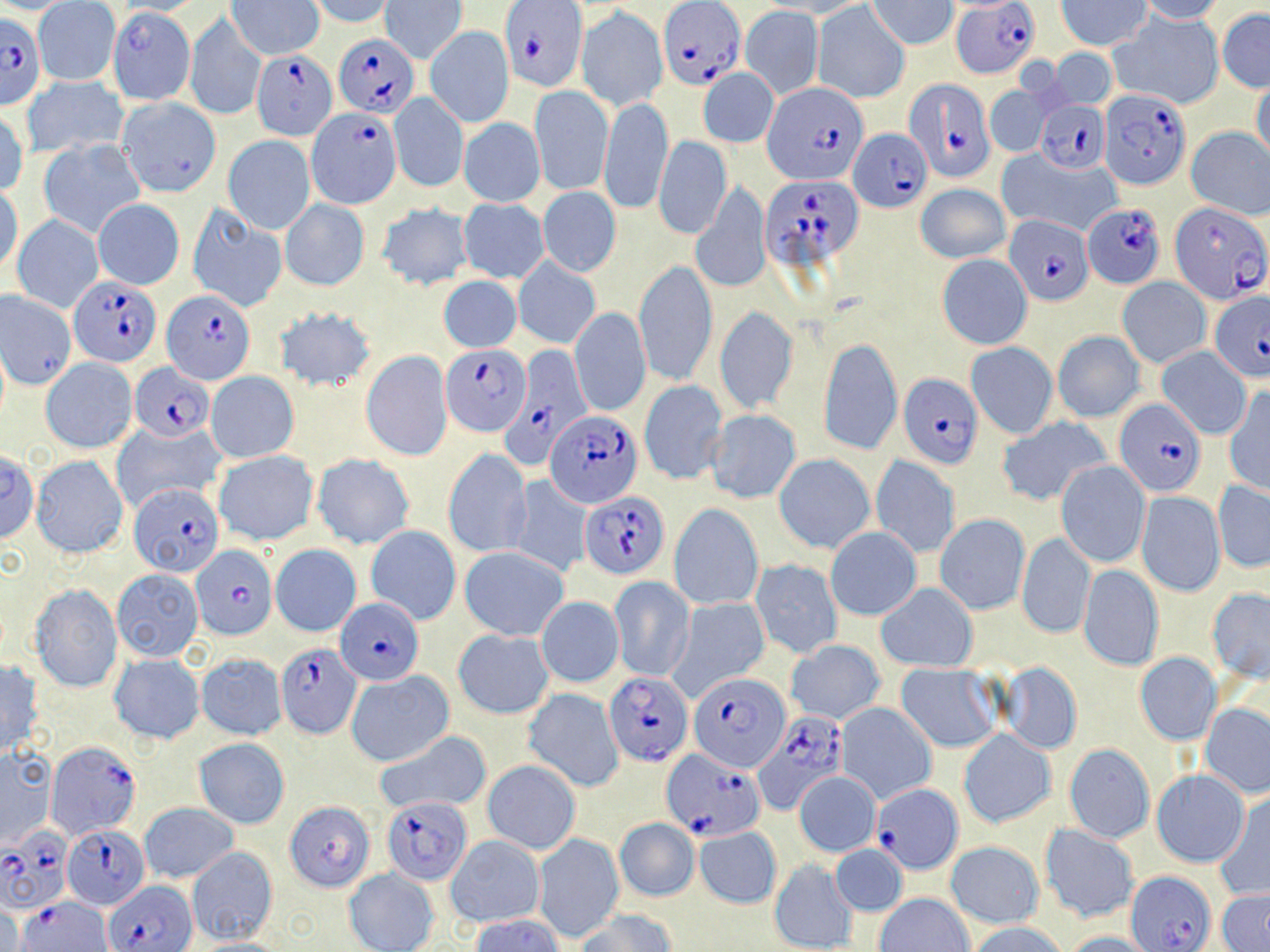
Summary:
  - Coordinate format: approximate bounding boxes as named x1/y1/x2/y2 corners in pixels
  - Plasmodium falciparum-infected red blood cell locations (subset): (x1=659, y1=0, x2=745, y2=88), (x1=500, y1=1, x2=586, y2=93), (x1=955, y1=1, x2=1037, y2=79), (x1=0, y1=11, x2=45, y2=111), (x1=333, y1=34, x2=419, y2=117), (x1=253, y1=49, x2=338, y2=141), (x1=764, y1=80, x2=866, y2=184), (x1=904, y1=80, x2=996, y2=185), (x1=1100, y1=89, x2=1193, y2=190), (x1=1036, y1=99, x2=1110, y2=176), (x1=309, y1=109, x2=400, y2=207), (x1=848, y1=130, x2=932, y2=212), (x1=761, y1=176, x2=862, y2=271), (x1=1083, y1=200, x2=1165, y2=287), (x1=1169, y1=200, x2=1269, y2=311), (x1=1005, y1=214, x2=1095, y2=305), (x1=70, y1=276, x2=162, y2=367), (x1=161, y1=290, x2=253, y2=384), (x1=1209, y1=291, x2=1270, y2=382), (x1=511, y1=343, x2=599, y2=458), (x1=442, y1=346, x2=528, y2=435), (x1=129, y1=362, x2=215, y2=441), (x1=898, y1=373, x2=984, y2=469), (x1=1115, y1=398, x2=1207, y2=497), (x1=545, y1=409, x2=642, y2=509), (x1=127, y1=482, x2=224, y2=577), (x1=580, y1=492, x2=670, y2=578), (x1=191, y1=544, x2=277, y2=639), (x1=335, y1=597, x2=424, y2=684), (x1=275, y1=642, x2=362, y2=738), (x1=688, y1=672, x2=791, y2=771), (x1=604, y1=673, x2=693, y2=765), (x1=754, y1=711, x2=849, y2=814), (x1=45, y1=740, x2=142, y2=839), (x1=660, y1=750, x2=764, y2=840), (x1=872, y1=784, x2=963, y2=873), (x1=382, y1=798, x2=473, y2=885), (x1=284, y1=801, x2=375, y2=891), (x1=61, y1=826, x2=149, y2=909), (x1=0, y1=832, x2=71, y2=912), (x1=1126, y1=871, x2=1216, y2=951), (x1=105, y1=880, x2=194, y2=951), (x1=20, y1=897, x2=114, y2=952)
  - Uninfected red blood cell locations (subset): (x1=762, y1=0, x2=872, y2=17), (x1=1056, y1=0, x2=1152, y2=51), (x1=1134, y1=0, x2=1226, y2=23), (x1=227, y1=1, x2=323, y2=59), (x1=307, y1=1, x2=398, y2=27), (x1=380, y1=1, x2=466, y2=63), (x1=867, y1=1, x2=956, y2=47), (x1=33, y1=2, x2=120, y2=85), (x1=740, y1=5, x2=822, y2=100), (x1=813, y1=5, x2=909, y2=103), (x1=107, y1=7, x2=194, y2=105), (x1=576, y1=7, x2=668, y2=112), (x1=1110, y1=7, x2=1225, y2=111), (x1=1216, y1=9, x2=1270, y2=93), (x1=185, y1=14, x2=265, y2=121), (x1=424, y1=26, x2=514, y2=128), (x1=1048, y1=49, x2=1117, y2=110), (x1=698, y1=68, x2=779, y2=149), (x1=21, y1=75, x2=127, y2=159), (x1=1250, y1=77, x2=1269, y2=167), (x1=985, y1=84, x2=1053, y2=157), (x1=530, y1=85, x2=614, y2=195), (x1=389, y1=93, x2=468, y2=194), (x1=599, y1=95, x2=672, y2=216), (x1=116, y1=97, x2=222, y2=197), (x1=1, y1=108, x2=28, y2=196), (x1=459, y1=119, x2=545, y2=207), (x1=1184, y1=126, x2=1270, y2=219), (x1=223, y1=134, x2=316, y2=234), (x1=653, y1=137, x2=731, y2=240), (x1=38, y1=138, x2=145, y2=239), (x1=998, y1=149, x2=1122, y2=237), (x1=692, y1=180, x2=772, y2=295), (x1=0, y1=183, x2=22, y2=277), (x1=916, y1=183, x2=1009, y2=264), (x1=537, y1=186, x2=621, y2=277), (x1=93, y1=198, x2=185, y2=290), (x1=457, y1=198, x2=549, y2=284), (x1=280, y1=199, x2=369, y2=291), (x1=186, y1=202, x2=287, y2=312), (x1=375, y1=202, x2=474, y2=292), (x1=12, y1=214, x2=104, y2=312), (x1=937, y1=255, x2=1032, y2=350), (x1=513, y1=258, x2=601, y2=348), (x1=633, y1=263, x2=718, y2=386), (x1=439, y1=275, x2=521, y2=352), (x1=1118, y1=277, x2=1210, y2=369), (x1=583, y1=285, x2=705, y2=402), (x1=273, y1=305, x2=378, y2=393), (x1=570, y1=306, x2=650, y2=417), (x1=713, y1=308, x2=799, y2=416), (x1=1052, y1=331, x2=1146, y2=423), (x1=820, y1=337, x2=903, y2=457), (x1=966, y1=342, x2=1058, y2=438), (x1=1155, y1=346, x2=1252, y2=439), (x1=361, y1=350, x2=452, y2=460), (x1=41, y1=358, x2=137, y2=454), (x1=206, y1=370, x2=300, y2=464), (x1=638, y1=380, x2=727, y2=486), (x1=1223, y1=386, x2=1270, y2=494), (x1=705, y1=410, x2=801, y2=504), (x1=995, y1=417, x2=1111, y2=507), (x1=112, y1=419, x2=225, y2=514), (x1=443, y1=449, x2=532, y2=558), (x1=213, y1=450, x2=319, y2=546), (x1=0, y1=453, x2=40, y2=542), (x1=311, y1=453, x2=415, y2=550), (x1=773, y1=453, x2=875, y2=555), (x1=30, y1=455, x2=129, y2=557), (x1=871, y1=455, x2=960, y2=558), (x1=1055, y1=460, x2=1150, y2=568), (x1=508, y1=476, x2=592, y2=579), (x1=1213, y1=481, x2=1270, y2=573), (x1=1137, y1=491, x2=1225, y2=596), (x1=669, y1=504, x2=763, y2=611), (x1=934, y1=514, x2=1030, y2=615), (x1=366, y1=525, x2=460, y2=624), (x1=825, y1=527, x2=921, y2=619), (x1=1016, y1=531, x2=1095, y2=640), (x1=271, y1=545, x2=361, y2=637), (x1=460, y1=547, x2=568, y2=641), (x1=750, y1=558, x2=843, y2=657), (x1=1078, y1=564, x2=1163, y2=673), (x1=111, y1=569, x2=203, y2=661), (x1=608, y1=576, x2=695, y2=683), (x1=877, y1=582, x2=977, y2=672), (x1=29, y1=583, x2=123, y2=693), (x1=1205, y1=587, x2=1268, y2=681), (x1=536, y1=595, x2=624, y2=687), (x1=671, y1=597, x2=771, y2=698), (x1=452, y1=629, x2=554, y2=719), (x1=786, y1=643, x2=885, y2=723), (x1=1135, y1=653, x2=1222, y2=746), (x1=109, y1=654, x2=203, y2=744), (x1=196, y1=654, x2=287, y2=740), (x1=1, y1=658, x2=44, y2=757), (x1=995, y1=661, x2=1083, y2=755), (x1=895, y1=662, x2=1002, y2=752), (x1=346, y1=672, x2=453, y2=767), (x1=523, y1=688, x2=624, y2=792), (x1=835, y1=702, x2=937, y2=805), (x1=1201, y1=703, x2=1270, y2=797), (x1=959, y1=730, x2=1055, y2=828), (x1=375, y1=731, x2=492, y2=812), (x1=193, y1=737, x2=290, y2=828), (x1=1064, y1=743, x2=1155, y2=844), (x1=0, y1=748, x2=56, y2=850), (x1=482, y1=761, x2=580, y2=855), (x1=1151, y1=769, x2=1250, y2=868), (x1=794, y1=771, x2=880, y2=857), (x1=1214, y1=794, x2=1270, y2=899), (x1=140, y1=803, x2=238, y2=883), (x1=614, y1=818, x2=698, y2=902), (x1=1039, y1=825, x2=1138, y2=924), (x1=694, y1=826, x2=781, y2=909), (x1=445, y1=834, x2=545, y2=928), (x1=534, y1=834, x2=624, y2=943), (x1=946, y1=840, x2=1044, y2=929), (x1=831, y1=843, x2=907, y2=918), (x1=186, y1=846, x2=278, y2=943), (x1=769, y1=859, x2=857, y2=951), (x1=343, y1=867, x2=439, y2=952), (x1=1216, y1=889, x2=1270, y2=950), (x1=875, y1=892, x2=974, y2=952), (x1=579, y1=911, x2=676, y2=952), (x1=470, y1=912, x2=565, y2=952), (x1=970, y1=922, x2=1067, y2=952), (x1=1062, y1=930, x2=1159, y2=951)
  - Slide-level diagnosis: Plasmodium falciparum
  - Image size: 1270×952 pixels
  - Stain: May-Grünwald-Giemsa
  - Field of view: one of a larger specimen
  - Magnification: 1000x
  - Preparation: thin blood film
  - Modality: optical microscopy